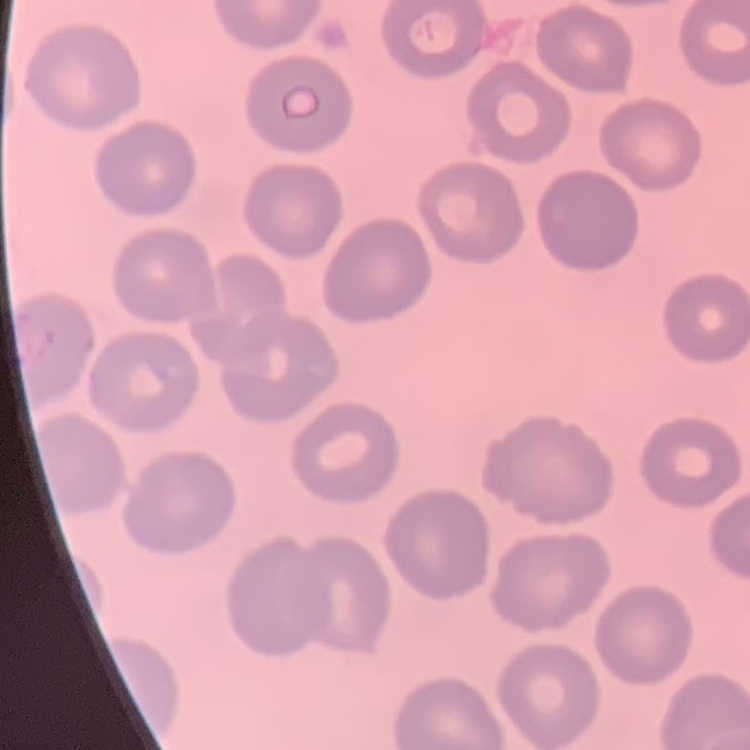
The erythrocytes exhibit no rouleaux formation. Field's or Giemsa stain. Thin blood smear. Square crop of a larger photomicrograph.